Point out leukocytes.
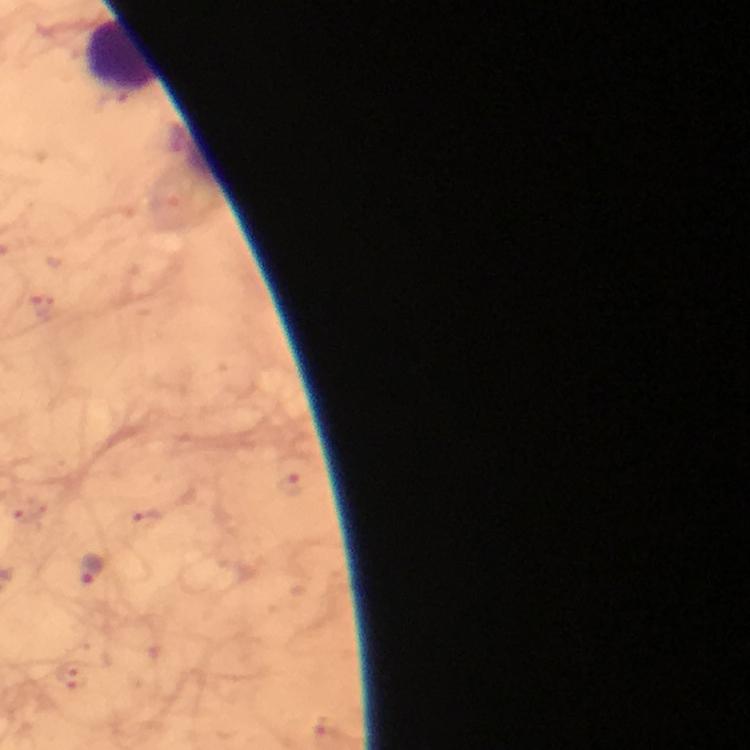
Approximate centers as {x, y} in pixels.
Leukocytes: {122, 56}.

Malaria parasite locations: {90, 569}. Giemsa stain. Image is 750×750 pixels. Immersion oil applied. From a diagnostic examination for malaria. At 100x magnification. A crop from one field of view. Thick blood film. Photographed with a smartphone mounted on the microscope.